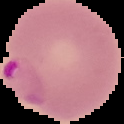

preparation: thin blood smear
image_size: 124×124 pixels
malaria_status: parasitized
image_type: segmented cell region on a black background